Give the location of every parasitized RBC.
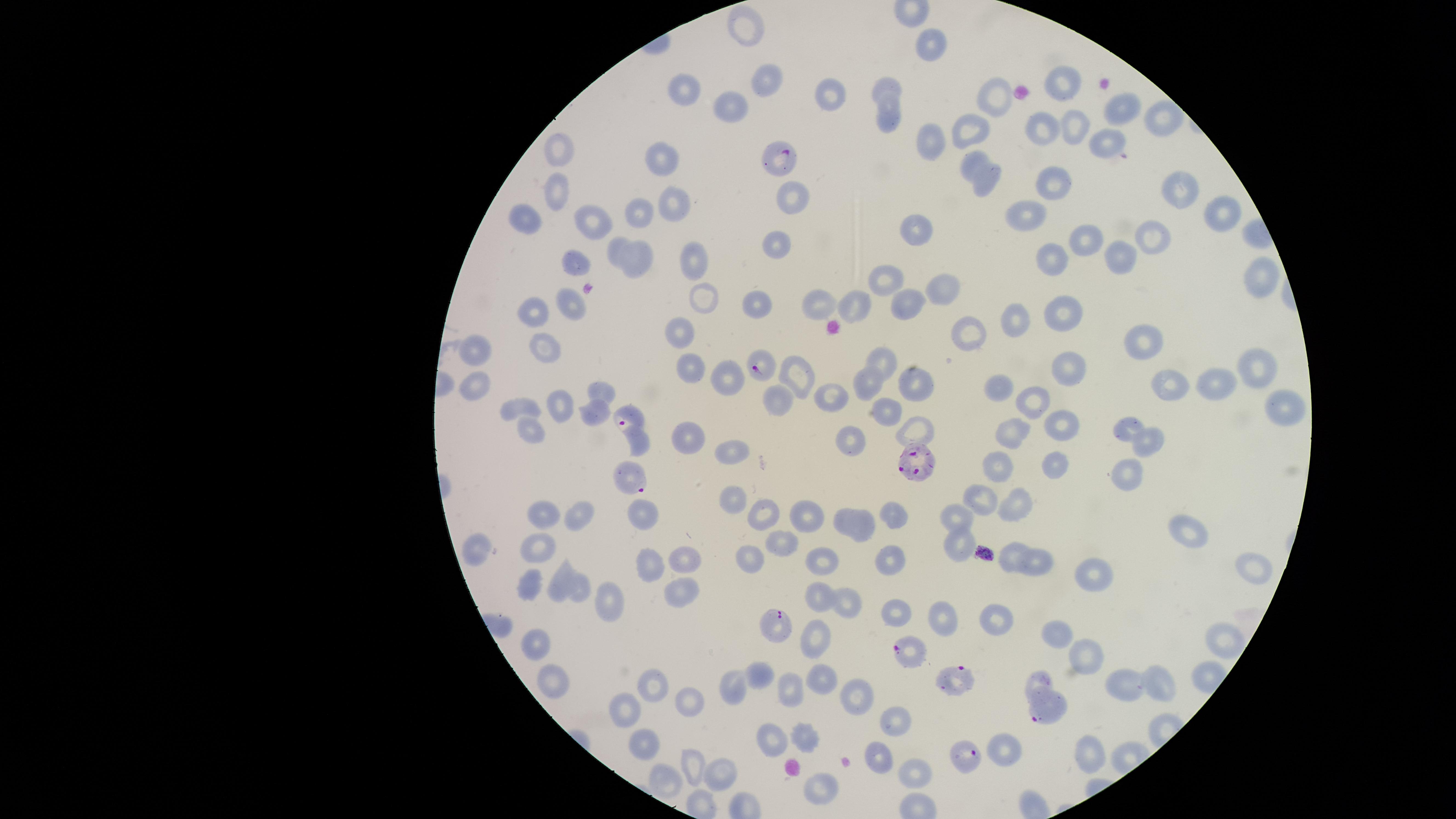

Approximate marker points as (x, y) in pixels.
Parasitized RBCs: (782, 158), (765, 364), (628, 417), (917, 462), (631, 478), (775, 623), (908, 649), (953, 682), (1047, 707), (967, 756).

{
  "image_size": "1456×819 pixels",
  "capture": "smartphone photograph through the microscope eyepiece",
  "uninfected_RBCs": "approximate marker points as (x, y) in pixels: (755, 28), (932, 39), (771, 78), (1059, 80), (891, 86), (692, 91), (830, 91), (997, 102), (736, 104), (1124, 107), (1161, 107), (889, 120), (1072, 124), (1040, 130), (974, 132), (932, 140), (1107, 141), (563, 146), (669, 158), (975, 158), (1048, 177), (985, 184), (1180, 187), (562, 188), (789, 193), (1219, 206), (1032, 210), (674, 212), (634, 215), (524, 216), (593, 216), (918, 228), (1093, 238), (1153, 240), (775, 241), (621, 246), (1123, 253), (1053, 258), (578, 260), (695, 260), (638, 261), (1262, 273), (882, 283), (941, 286), (703, 299), (822, 301), (761, 302), (909, 302), (573, 304), (856, 309), (537, 310), (1071, 315), (1019, 317), (967, 327), (682, 329), (1139, 344), (551, 350), (474, 351), (886, 361), (692, 363), (1257, 366), (1070, 368), (786, 371), (789, 372), (730, 376), (1215, 382), (1168, 384), (864, 385), (915, 386), (477, 387), (609, 388), (996, 391), (1032, 398), (1285, 400), (784, 401), (831, 402), (523, 404), (564, 404), (889, 411), (590, 417), (1066, 426), (1127, 426), (529, 427), (922, 430), (1011, 430), (688, 432), (1155, 436), (851, 438), (639, 446), (733, 453), (1001, 466), (1056, 466), (1129, 473), (735, 493), (985, 500), (1014, 503), (763, 506), (546, 510), (895, 510), (643, 511), (577, 512), (804, 514), (842, 516), (957, 516), (861, 525), (1191, 531), (783, 539), (961, 545), (539, 547), (479, 553), (1014, 554), (684, 555), (749, 556), (824, 557), (653, 559), (893, 564), (1042, 564), (1256, 569), (1097, 573), (560, 578), (534, 581), (581, 589), (682, 590), (815, 596), (618, 599), (842, 602), (998, 615), (945, 616), (1059, 631), (814, 640), (1222, 640), (538, 641), (1088, 654), (819, 676), (554, 679), (1040, 679), (1164, 681), (650, 684), (1128, 688), (790, 695), (859, 696), (689, 698), (627, 705), (893, 720), (803, 734), (771, 736), (643, 741), (1008, 752), (1094, 752), (876, 753), (694, 763), (918, 767), (725, 770), (663, 777), (821, 788)",
  "field_of_view": "single",
  "stain": "Giemsa",
  "species": "Plasmodium falciparum",
  "visible_region": "circular",
  "preparation": "thin blood film"
}